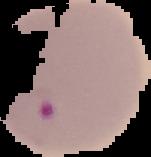 Malaria status: parasitized. Image is 151×157 pixels. Segmented cell region on a black background. From a thin blood film.